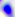
Micrograph. 400x magnification. Toxoplasma gondii is seen.